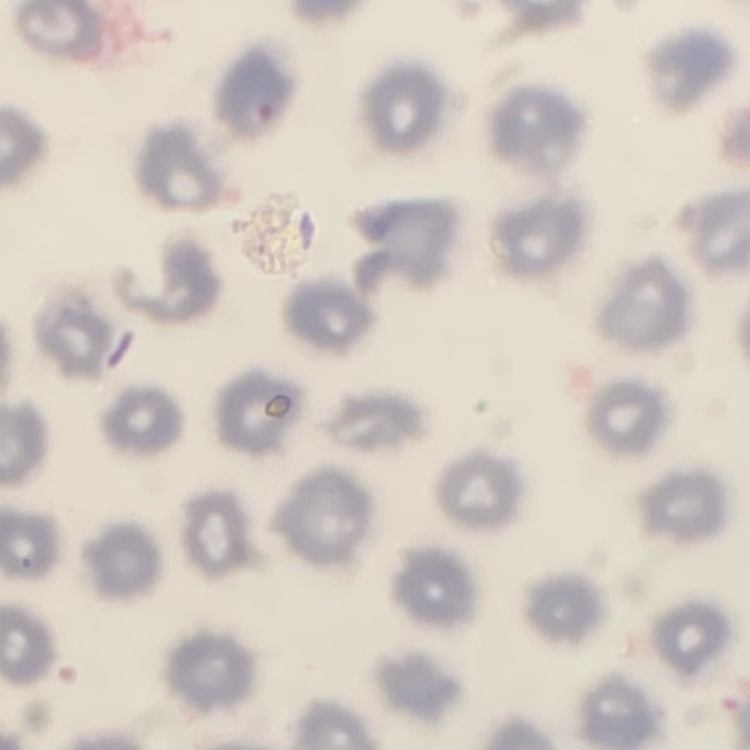
erythrocyte morphology = no rouleaux formation
image type = one tile cut from a larger photomicrograph
stain = Field's or Giemsa
preparation = thin blood film